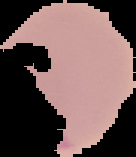

preparation = thin blood film
image size = 136×157 pixels
malaria status = parasitized
image type = cell region segmented out of the field of view; surrounding area masked to black